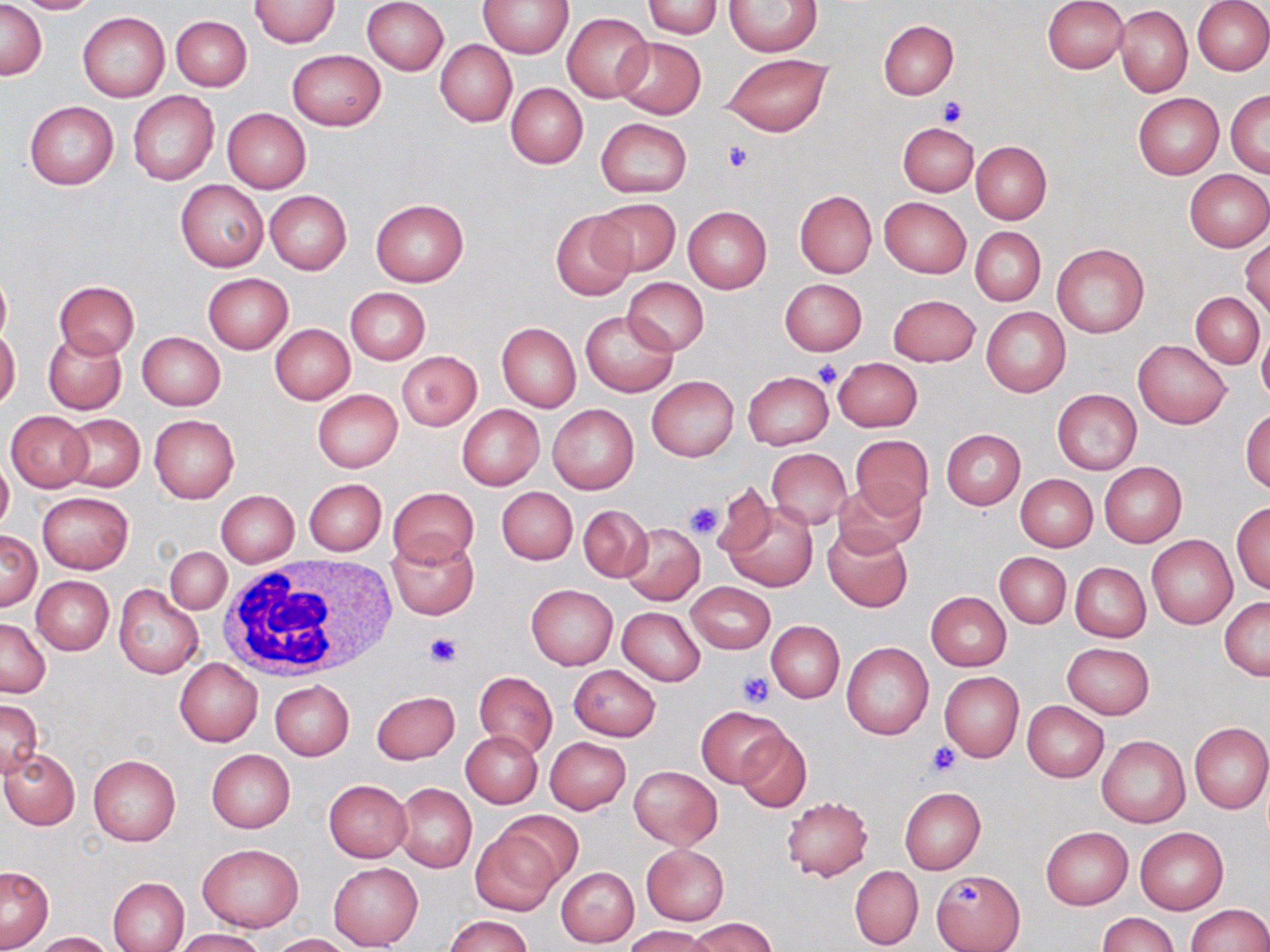

Summary:
  - Coordinate format: approximate bounding boxes as (x1,y1)-(x2,y2) corner pairs in pixels
  - White blood cell locations: (215,557)-(397,682)
  - Platelet locations: (936,97)-(966,126), (722,140)-(753,172), (813,362)-(841,386), (685,501)-(723,539), (422,632)-(463,670), (738,672)-(775,707), (927,742)-(960,774), (953,880)-(984,910)
  - Uninfected red blood cell locations: (0,0)-(46,79), (12,0)-(101,14), (250,0)-(341,48), (361,0)-(448,75), (477,0)-(574,57), (643,0)-(722,38), (1042,0)-(1128,74), (1192,0)-(1270,75), (726,1)-(822,56), (1114,5)-(1192,97), (77,12)-(170,102), (562,12)-(652,103), (170,15)-(252,91), (878,20)-(957,99), (614,36)-(706,119), (436,41)-(516,127), (287,50)-(386,131), (723,53)-(833,135), (505,83)-(587,168), (1226,89)-(1270,176), (127,91)-(219,186), (1133,93)-(1222,180), (24,101)-(119,189), (222,108)-(311,193), (595,118)-(691,196), (899,122)-(978,195), (971,141)-(1052,224), (1184,169)-(1269,251), (176,180)-(268,272), (795,190)-(876,278), (264,191)-(351,275), (879,197)-(970,278), (590,198)-(681,277), (370,199)-(469,286), (682,206)-(771,293), (550,210)-(635,300), (971,227)-(1046,305), (1241,239)-(1269,318), (1052,242)-(1149,338), (0,268)-(12,348), (202,274)-(293,353), (621,277)-(709,356), (780,278)-(866,355), (55,281)-(139,358), (345,287)-(430,364), (1192,292)-(1265,368), (888,294)-(980,366), (983,307)-(1070,396), (580,309)-(678,397), (497,323)-(580,411), (271,324)-(355,404), (1257,325)-(1270,406), (0,327)-(20,409), (42,331)-(126,414), (136,331)-(226,410), (1134,339)-(1230,429), (398,351)-(482,431), (833,357)-(922,432), (743,371)-(833,449), (647,376)-(739,461), (1052,388)-(1141,474), (312,389)-(403,472), (548,404)-(638,494), (456,405)-(544,491), (1241,408)-(1270,495), (6,411)-(92,492), (60,413)-(145,492), (149,415)-(239,503), (941,429)-(1025,509), (850,436)-(934,515), (766,448)-(852,529), (0,457)-(14,531), (1099,462)-(1187,547), (1015,474)-(1098,550), (305,479)-(386,556), (832,479)-(924,558), (710,481)-(779,561), (387,487)-(478,567), (497,487)-(577,564), (215,490)-(299,567), (37,492)-(133,573), (720,497)-(819,592), (1232,501)-(1270,595), (578,505)-(652,582), (620,522)-(705,607), (823,525)-(912,612), (1,530)-(41,611), (384,535)-(479,620), (1147,535)-(1237,630), (166,547)-(231,614), (995,552)-(1070,630), (1069,561)-(1152,642), (31,576)-(114,655), (686,582)-(775,653), (112,583)-(205,680), (526,584)-(617,669), (926,591)-(1012,670), (1220,596)-(1270,680), (618,607)-(705,685), (0,618)-(50,698), (767,621)-(844,702), (842,642)-(934,740), (1062,642)-(1153,719), (175,659)-(262,746), (568,664)-(661,740), (473,671)-(557,759), (940,672)-(1023,761), (270,680)-(355,761), (372,690)-(459,765), (0,700)-(42,777), (1022,700)-(1109,782), (697,705)-(788,787), (1189,722)-(1270,813), (734,728)-(811,813), (461,731)-(544,807), (1097,736)-(1190,828), (545,737)-(632,814), (1,749)-(79,830), (206,749)-(295,832), (87,753)-(181,846), (628,765)-(722,850), (324,780)-(412,862), (395,783)-(476,873), (899,787)-(986,873), (781,796)-(872,881), (493,811)-(584,888), (1040,826)-(1133,909), (1134,827)-(1228,914), (471,832)-(560,916), (197,843)-(303,931), (641,845)-(729,925), (329,863)-(423,950), (850,866)-(923,949), (1,867)-(54,950), (556,867)-(639,947), (932,869)-(1025,950), (107,877)-(189,952), (1185,903)-(1270,951), (1098,913)-(1179,952), (445,914)-(532,952), (690,917)-(775,952), (624,926)-(715,952), (171,929)-(267,951), (31,931)-(115,952), (270,933)-(351,952)
  - Slide-level diagnosis: no evidence of blood parasites
  - Preparation: thin blood film
  - Magnification: 1000x
  - Modality: light microscopy
  - Image size: 1270×952 pixels
  - Field of view: one of a larger specimen
  - Stain: May-Grünwald-Giemsa